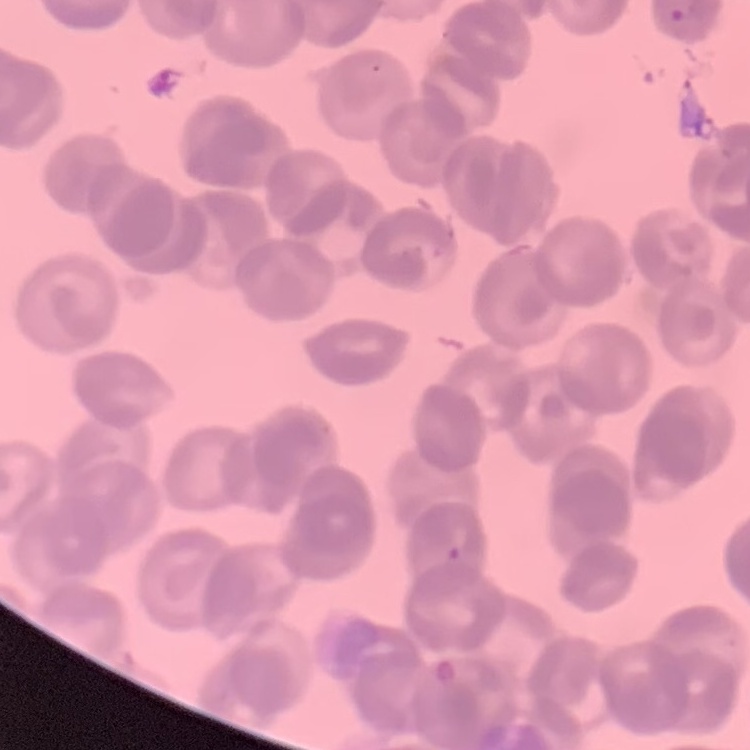
Summary:
  - Red blood cell morphology: rouleaux formation
  - Image type: one tile cut from a larger photomicrograph
  - Preparation: thin blood smear
  - Stain: Field's or Giemsa